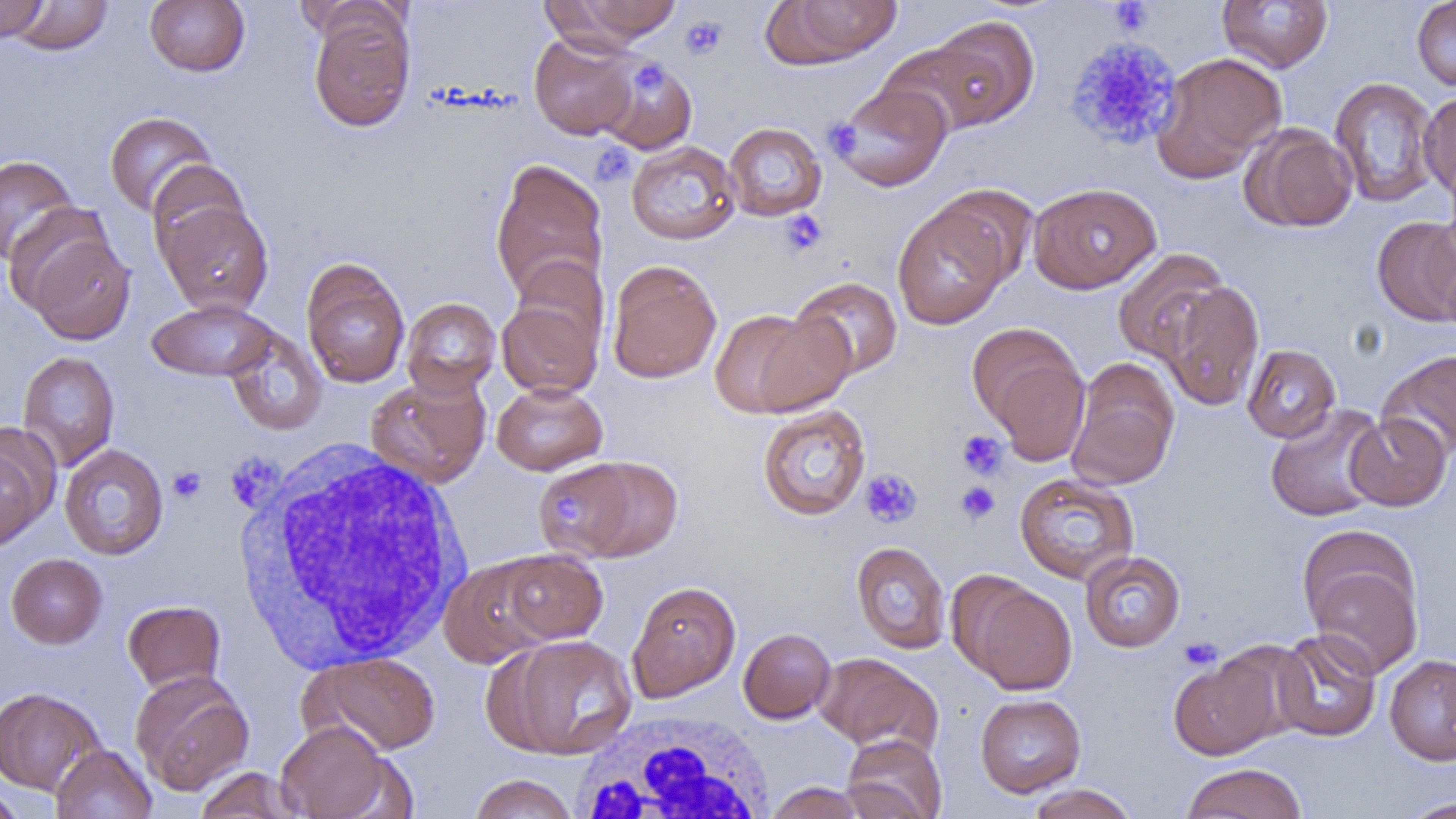 Approximate bounding boxes as (x1,y1)-(x2,y2) corner pairs in pixels. Uninfected red blood cell locations: (0,0)-(47,43), (9,0)-(113,56), (144,0)-(250,76), (294,0)-(411,46), (554,0)-(686,44), (765,0)-(903,68), (1217,1)-(1333,74), (1411,1)-(1456,91), (307,6)-(416,133), (925,15)-(1040,131), (529,32)-(640,140), (876,41)-(1004,138), (1151,52)-(1286,183), (595,56)-(698,154), (1329,76)-(1440,208), (831,82)-(952,192), (1418,91)-(1456,202), (103,111)-(217,217), (724,122)-(827,221), (1242,123)-(1358,232), (626,141)-(741,245), (0,154)-(80,266), (490,157)-(609,305), (146,160)-(250,261), (1028,182)-(1161,293), (932,183)-(1040,288), (154,198)-(274,316), (893,202)-(1009,329), (1428,210)-(1456,328), (1372,216)-(1456,326), (16,220)-(136,345), (1112,248)-(1230,365), (510,256)-(610,356), (301,258)-(410,388), (606,259)-(722,383), (791,276)-(903,380), (1161,280)-(1265,410), (496,292)-(605,400), (401,297)-(501,398), (147,299)-(277,382), (711,306)-(852,417), (223,326)-(327,436), (972,329)-(1091,464), (1242,344)-(1341,443), (1378,349)-(1456,461), (17,351)-(120,471), (1066,358)-(1180,490), (366,373)-(491,488), (491,381)-(608,476), (1265,403)-(1389,522), (756,404)-(871,521), (1345,413)-(1451,511), (0,428)-(53,551), (59,444)-(169,560), (533,459)-(650,559), (1015,472)-(1139,585), (1300,536)-(1425,678), (851,541)-(951,654), (497,549)-(608,645), (1079,550)-(1186,652), (6,553)-(107,648), (439,555)-(557,667), (627,580)-(742,702), (962,581)-(1078,695), (122,599)-(226,694), (738,627)-(836,723), (1272,629)-(1382,742), (499,634)-(637,759), (1209,641)-(1315,747), (302,652)-(442,756), (814,652)-(940,754), (1168,653)-(1283,760), (1384,654)-(1456,765), (130,670)-(254,795), (0,686)-(106,796), (975,693)-(1086,797), (275,720)-(397,818), (841,734)-(947,819), (51,744)-(157,819), (1180,762)-(1307,819), (193,767)-(304,819), (468,774)-(579,819), (764,781)-(867,819), (0,784)-(26,819), (1026,784)-(1138,819), (1399,796)-(1456,818). Platelet locations: (1108,1)-(1153,35), (681,15)-(727,59), (1064,36)-(1183,151), (629,61)-(667,98), (824,119)-(863,158), (590,143)-(638,187), (778,210)-(828,257), (956,430)-(1009,480), (225,454)-(283,513), (168,466)-(206,503), (860,469)-(922,528), (955,481)-(1000,524), (551,495)-(585,525), (1179,637)-(1223,670). White blood cell locations: (232,441)-(473,671), (570,711)-(777,819). Slide-level diagnosis: negative for blood parasites. Thin blood film. One field of a larger specimen. Optical microscopy. Image is 1456×819 pixels. 1000x magnification.